Locate platelets.
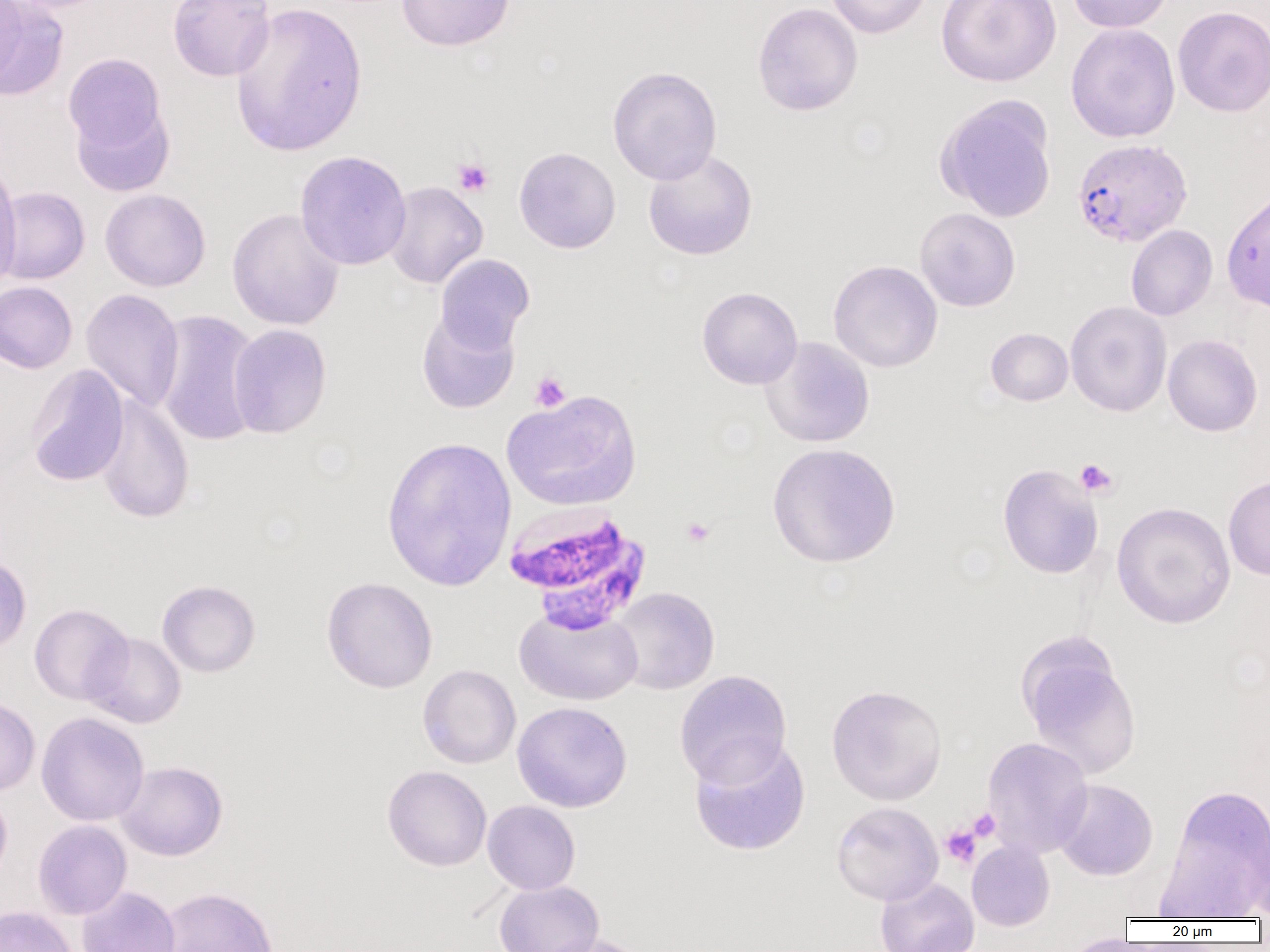

Approximate bounding boxes as (x1, y1, x2, y2) in pixels.
Platelets: (452, 157, 494, 197), (529, 371, 571, 413), (1074, 458, 1119, 498), (681, 517, 715, 547), (967, 808, 1000, 842), (940, 825, 981, 868).

Uninfected red blood cell locations: (0, 0, 28, 86), (4, 0, 114, 13), (168, 0, 275, 82), (397, 0, 515, 52), (826, 0, 931, 39), (936, 0, 1061, 87), (1066, 0, 1174, 33), (1, 1, 69, 100), (230, 1, 367, 157), (752, 2, 863, 117), (1172, 5, 1270, 117), (1065, 23, 1181, 143), (64, 53, 168, 158), (607, 66, 722, 184), (936, 95, 1058, 222), (71, 101, 174, 198), (513, 147, 621, 254), (643, 149, 758, 260), (294, 150, 412, 270), (0, 159, 22, 292), (383, 181, 488, 289), (0, 187, 90, 284), (100, 189, 211, 292), (1221, 189, 1270, 313), (226, 207, 345, 331), (914, 207, 1020, 312), (1126, 225, 1217, 321), (434, 253, 535, 351), (828, 259, 943, 373), (0, 281, 77, 373), (697, 287, 802, 389), (81, 288, 184, 413), (1065, 301, 1172, 417), (416, 308, 520, 414), (153, 309, 262, 447), (227, 323, 332, 439), (986, 328, 1073, 406), (1163, 334, 1263, 437), (760, 336, 875, 448), (25, 364, 129, 488), (502, 389, 641, 511), (94, 393, 195, 525), (381, 435, 517, 591), (767, 442, 901, 568), (997, 463, 1104, 579), (1223, 475, 1270, 580), (1112, 501, 1236, 629), (0, 554, 31, 655), (321, 576, 438, 693), (157, 579, 260, 677), (609, 586, 720, 695), (29, 603, 134, 705), (514, 605, 644, 706), (83, 631, 186, 729), (1020, 645, 1141, 778), (418, 664, 521, 769), (674, 669, 792, 788), (826, 683, 948, 805), (0, 696, 40, 796), (512, 701, 632, 812), (36, 712, 149, 826), (981, 736, 1094, 859), (689, 738, 811, 857), (116, 761, 228, 861), (382, 765, 492, 871), (1053, 778, 1158, 881), (1158, 783, 1270, 918), (0, 789, 12, 888), (482, 800, 581, 895), (831, 801, 943, 906), (1247, 816, 1270, 922), (32, 820, 132, 919), (966, 839, 1055, 931), (875, 876, 979, 952), (494, 880, 604, 952), (77, 885, 180, 952), (157, 886, 279, 952), (0, 906, 78, 952), (535, 934, 652, 952), (1059, 934, 1145, 952). Plasmodium falciparum-infected red blood cell locations: (1072, 138, 1193, 248), (502, 502, 651, 628). Slide-level diagnosis: Plasmodium falciparum. Optical microscopy. Captured at 1000x magnification. Thin blood film. One field of a larger specimen. Image is 1270×952 pixels.